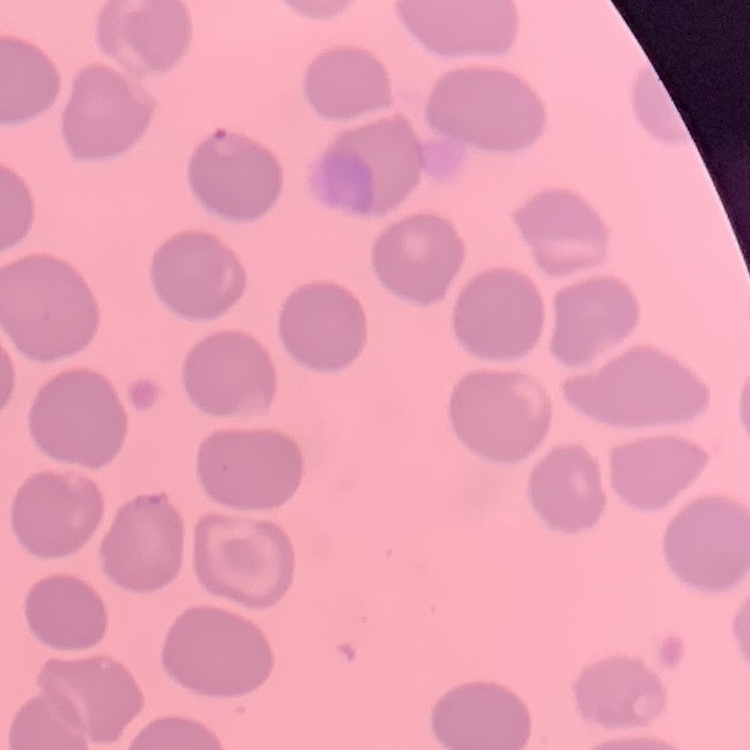 The erythrocytes exhibit no rouleaux formation. Stained with either Field's or Giemsa. One tile cut from a larger photomicrograph. Thin peripheral smear.